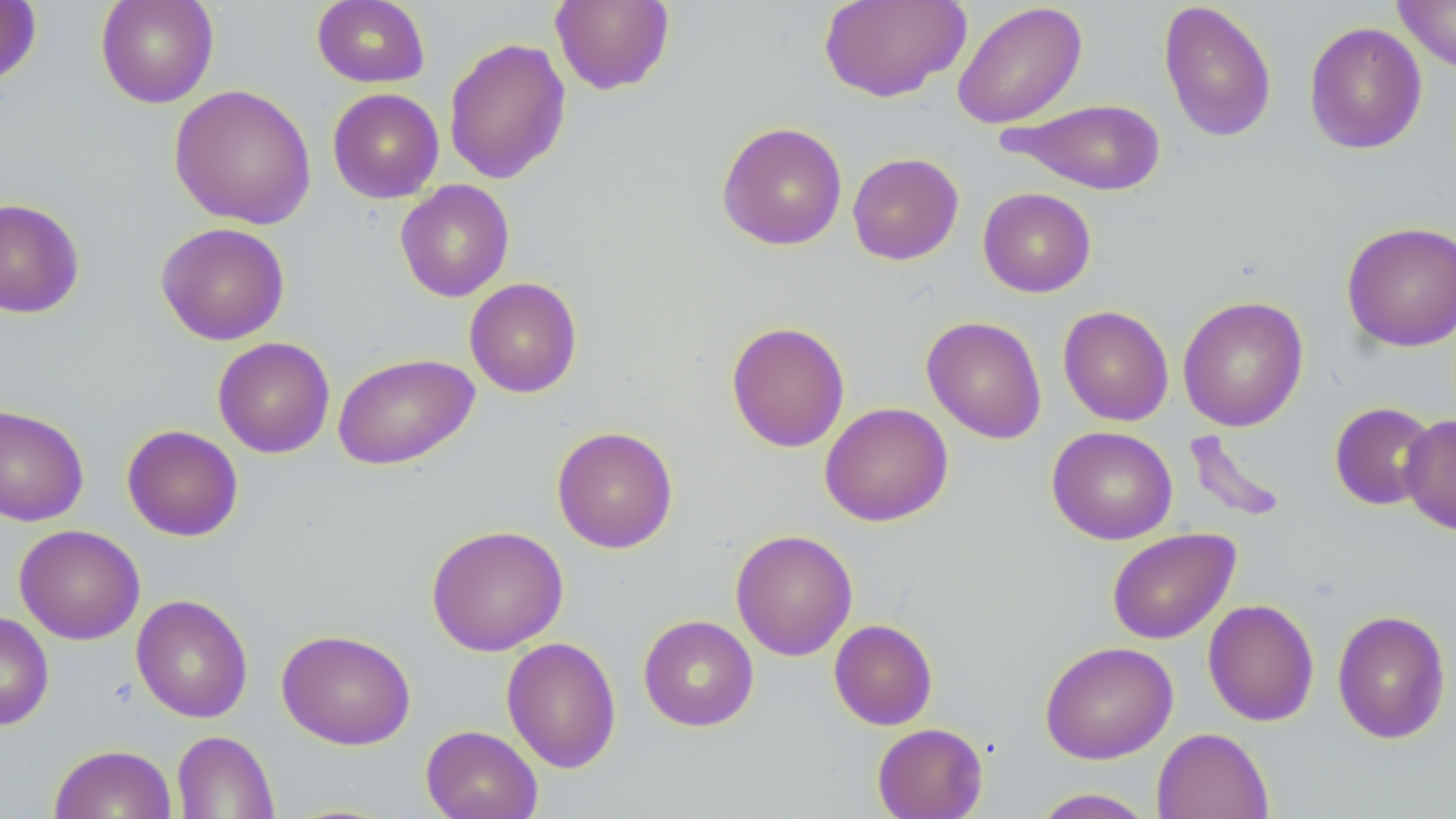
slide-level diagnosis = negative for blood parasites
image size = 1456×819 pixels
uninfected red blood cell locations = approximate bounding boxes as [x1, y1, x2, y2] in pixels: [95, 0, 219, 108], [311, 0, 430, 88], [819, 0, 970, 103], [1158, 0, 1277, 143], [1393, 0, 1456, 73], [0, 1, 42, 88], [550, 1, 675, 95], [951, 2, 1088, 130], [1303, 21, 1427, 154], [443, 37, 571, 185], [168, 84, 317, 230], [327, 88, 444, 203], [1003, 98, 1168, 195], [716, 121, 848, 251], [847, 152, 964, 265], [395, 179, 515, 302], [977, 187, 1096, 297], [0, 197, 85, 318], [1341, 221, 1456, 352], [155, 222, 290, 345], [464, 277, 583, 398], [1178, 295, 1309, 431], [1058, 305, 1174, 426], [921, 315, 1047, 444], [725, 320, 850, 453], [212, 337, 335, 458], [332, 352, 479, 470], [819, 402, 954, 527], [1329, 402, 1438, 511], [0, 404, 90, 527], [1399, 413, 1456, 536], [122, 424, 243, 541], [551, 426, 678, 553], [1047, 426, 1177, 545], [1182, 428, 1289, 525], [14, 524, 145, 645], [425, 524, 569, 656], [1106, 528, 1240, 644], [730, 529, 858, 661], [130, 593, 253, 723], [1202, 599, 1320, 726], [1332, 609, 1452, 744], [0, 610, 54, 731], [638, 614, 759, 732], [828, 619, 938, 730], [276, 628, 415, 750], [501, 636, 621, 773], [1040, 640, 1178, 763], [872, 722, 988, 818], [420, 724, 543, 819], [1152, 727, 1273, 819], [171, 730, 280, 818], [48, 744, 176, 819], [1031, 788, 1156, 818]
preparation = thin blood film
field of view = one of a larger specimen
modality = light microscopy
magnification = 1000x
stain = May-Grünwald-Giemsa